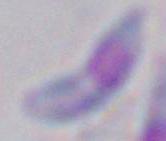
Summary:
  - Magnification: 1000x
  - Modality: photomicrograph
  - Identification: Toxoplasma gondii